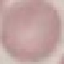

Result: negative for malaria parasites. Cell patch, automatically extracted from a larger field of view and resized to 64 × 64 pixels. Giemsa stain. Thin blood smear. Acquired by smartphone through the microscope eyepiece.